Comment on the morphology of the red blood cells.
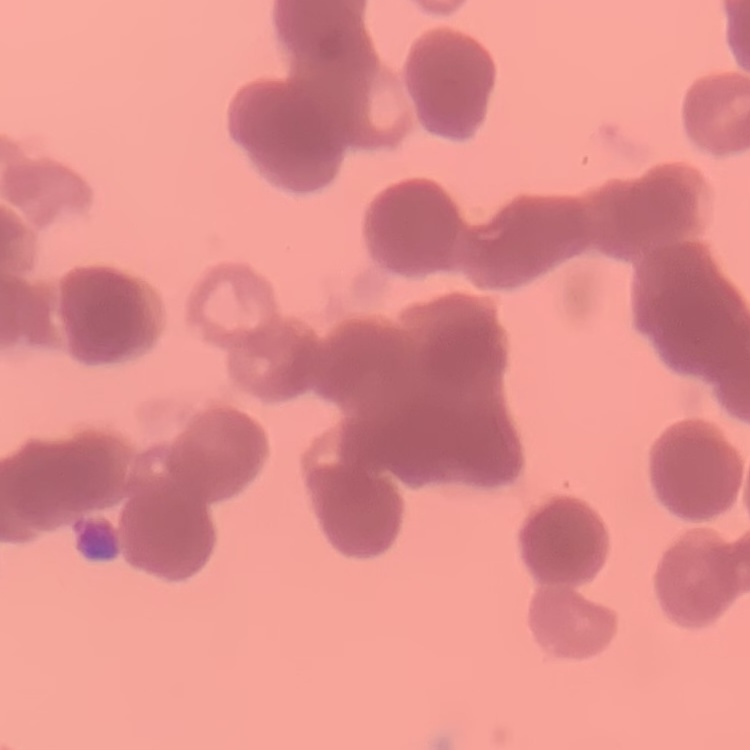
Rouleaux formation.

Summary:
  - Preparation: thin blood smear
  - Image type: one tile cut from a larger photomicrograph
  - Stain: Field's or Giemsa